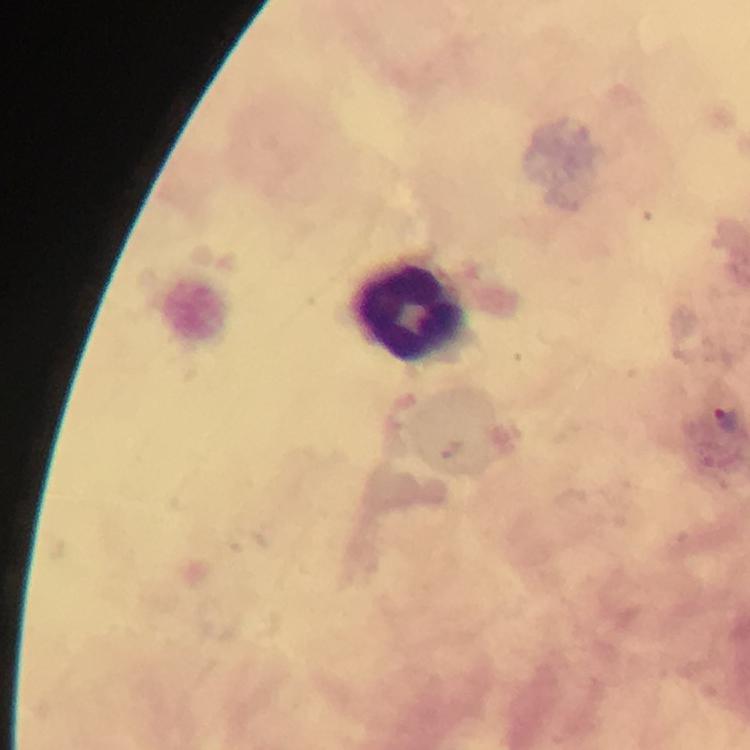

Approximate centers as {x, y} in pixels.
Summary:
  - Malaria parasite locations: {726, 420}
  - Leukocyte locations: {409, 313}
  - Cropped from: a single field of view
  - Stain: Giemsa
  - Context: from a malaria diagnostic workup
  - Magnification: 100x
  - Preparation: thick smear
  - Image size: 750×750 pixels
  - Immersion oil: used
  - Capture: smartphone camera through the microscope